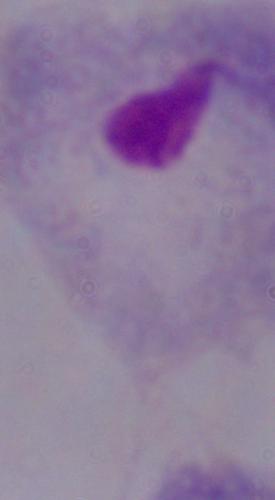

Summary:
  - Modality: micrograph
  - Identification: trichomonad
  - Magnification: 1000x